State which parasite is depicted.
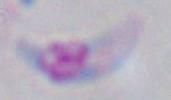

Toxoplasma gondii.

modality = photomicrograph
magnification = 1000x